Locate and identify every blood parasite.
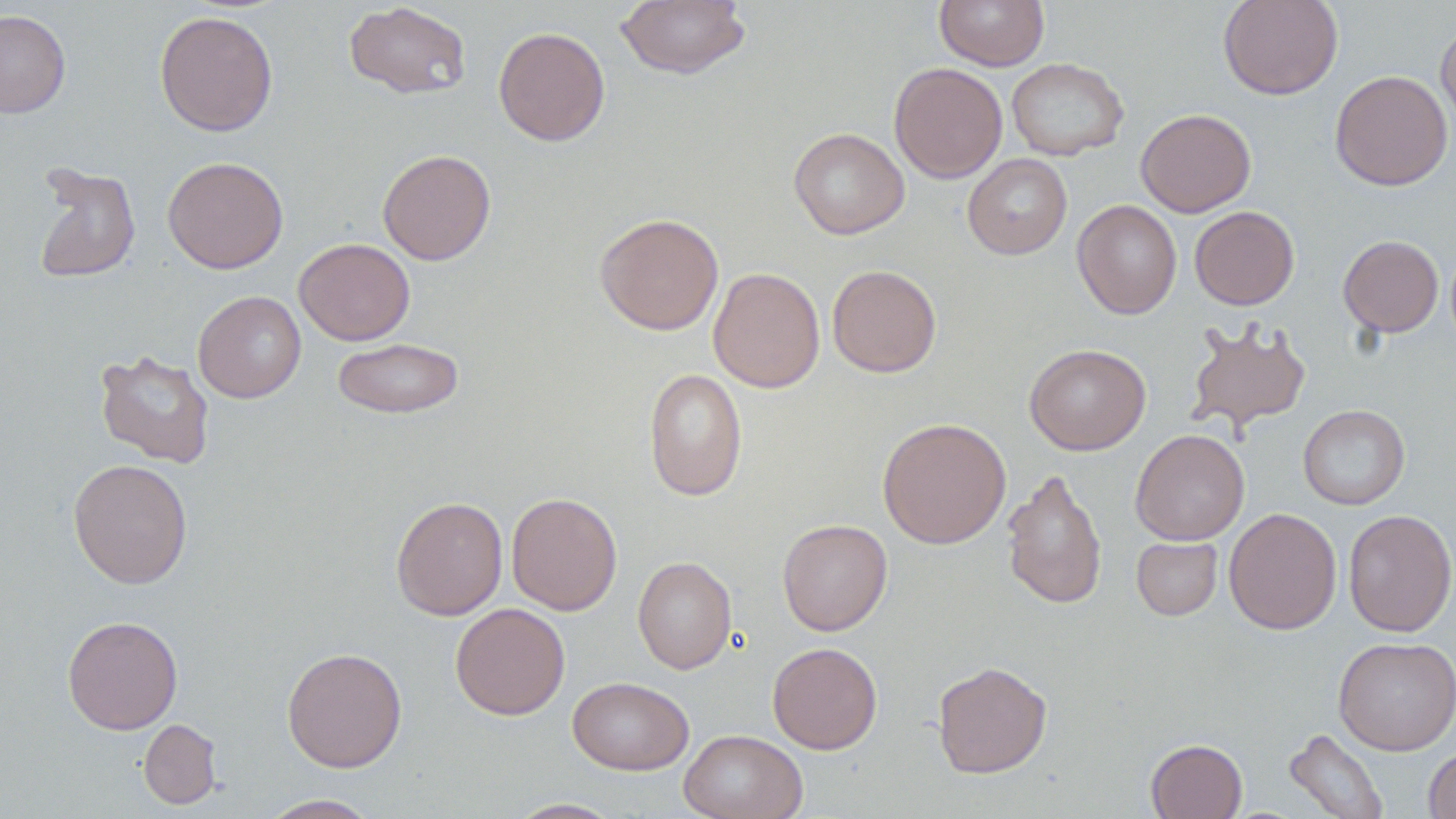

No blood parasites seen.

{
  "slide_level_diagnosis": "negative for blood parasites",
  "modality": "optical microscopy",
  "field_of_view": "single",
  "preparation": "thin blood film",
  "magnification": "1000x",
  "uninfected_red_blood_cell_locations": "approximate bounding boxes as (x1, y1, x2, y2) in pixels: (615, 0, 751, 80), (935, 0, 1049, 70), (1217, 0, 1344, 100), (343, 2, 472, 100), (0, 10, 71, 117), (154, 10, 278, 137), (1436, 20, 1456, 134), (493, 26, 610, 146), (1006, 57, 1129, 161), (888, 62, 1007, 183), (1330, 70, 1453, 191), (1135, 108, 1256, 217), (788, 128, 909, 239), (377, 149, 496, 265), (962, 154, 1073, 260), (162, 156, 288, 273), (31, 161, 142, 284), (1073, 199, 1182, 319), (1190, 206, 1300, 309), (594, 212, 724, 335), (1338, 234, 1443, 337), (294, 238, 415, 345), (826, 264, 942, 378), (708, 267, 825, 393), (193, 290, 306, 403), (1185, 319, 1312, 435), (332, 337, 464, 419), (1024, 343, 1151, 455), (94, 349, 216, 469), (643, 368, 748, 502), (1298, 404, 1410, 510), (877, 417, 1011, 548), (1130, 429, 1250, 545), (68, 458, 193, 589), (1001, 467, 1107, 610), (505, 492, 623, 616), (391, 496, 508, 620), (1224, 507, 1342, 635), (1342, 509, 1456, 637), (777, 518, 892, 636), (1131, 536, 1223, 620), (632, 555, 737, 675), (450, 602, 570, 720), (62, 615, 183, 734), (1333, 636, 1456, 755), (768, 642, 882, 754), (282, 646, 407, 772), (932, 661, 1052, 778), (567, 676, 694, 775), (139, 718, 222, 809), (679, 729, 807, 819), (1284, 729, 1389, 819), (1145, 738, 1247, 819), (1424, 746, 1456, 819), (257, 794, 382, 818), (507, 798, 625, 818)",
  "image_size": "1456×819 pixels",
  "stain": "May-Grünwald-Giemsa"
}